Classify this cell by malaria status.
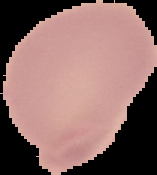

It is uninfected.

Cell region segmented out of the field of view; the surrounding area is masked to black. Image is 157×175 pixels. From a thin blood film.